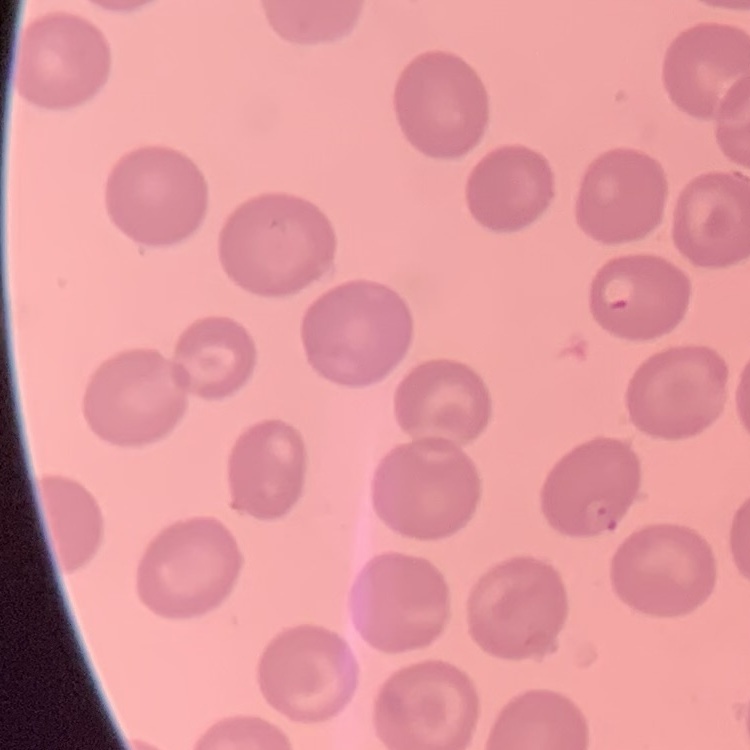 The red blood cells exhibit no rouleaux formation. Thin blood smear. One tile cut from a larger photomicrograph. Field's or Giemsa stain.